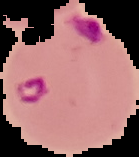

Summary:
  - Image type: segmented cell region on a black background
  - Result: Plasmodium parasites detected
  - Preparation: thin blood film
  - Image size: 139×157 pixels